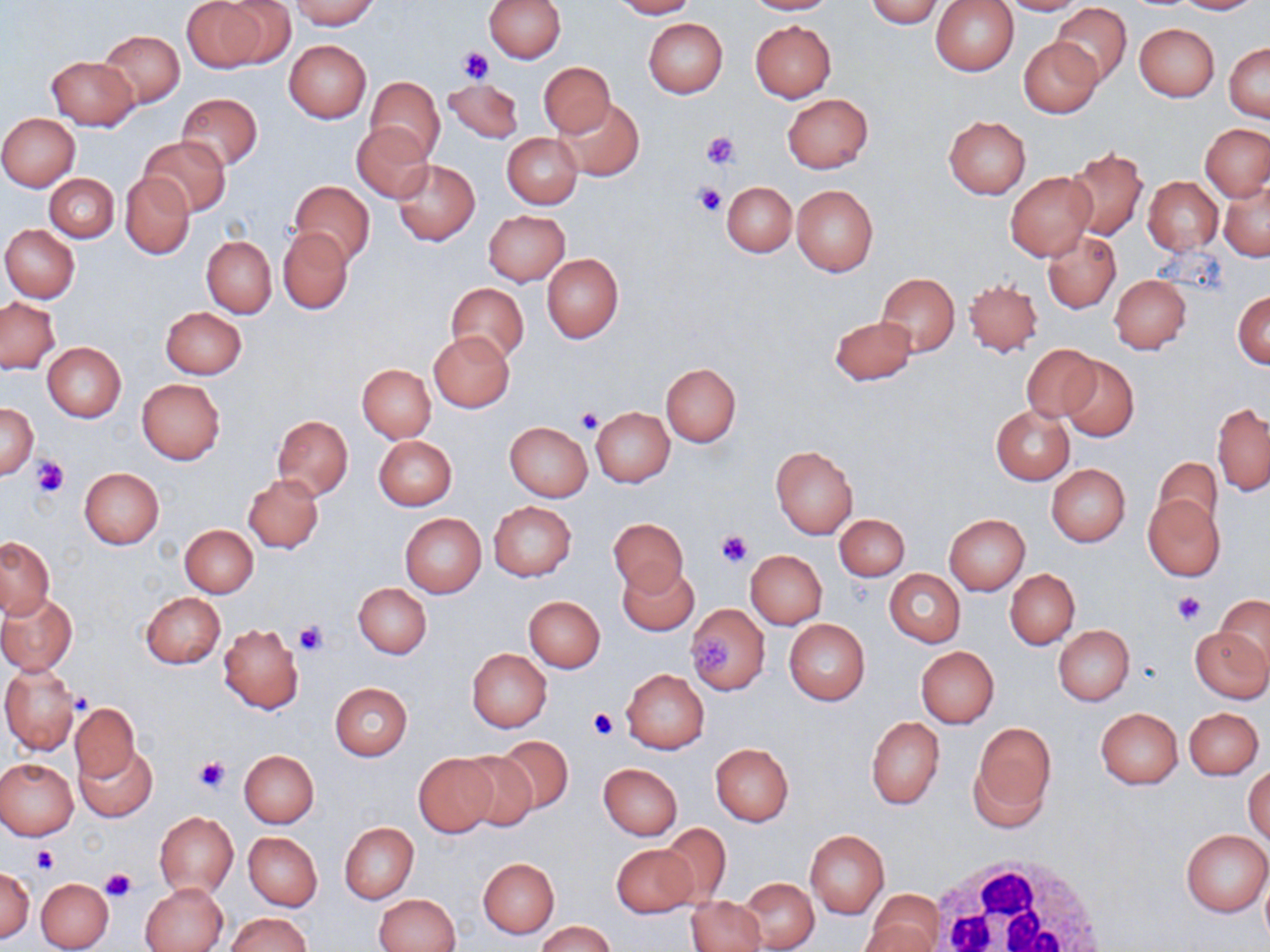
Summary:
  - Coordinate format: approximate bounding boxes as (x1, y1, x2, y2) in pixels
  - Uninfected red blood cell locations: (183, 0, 268, 72), (215, 0, 297, 68), (289, 0, 379, 30), (485, 0, 565, 62), (611, 0, 697, 18), (744, 0, 835, 15), (865, 0, 945, 27), (930, 0, 1019, 76), (998, 0, 1087, 15), (1174, 0, 1259, 14), (1050, 3, 1133, 87), (644, 19, 727, 99), (750, 21, 836, 102), (1134, 23, 1219, 100), (98, 29, 185, 108), (1019, 37, 1103, 117), (284, 40, 372, 123), (1225, 43, 1270, 122), (46, 56, 139, 130), (539, 62, 615, 137), (365, 76, 444, 162), (442, 78, 523, 144), (176, 92, 262, 172), (783, 93, 873, 173), (556, 97, 645, 181), (0, 113, 80, 191), (944, 116, 1031, 198), (352, 122, 433, 203), (1201, 123, 1269, 200), (502, 132, 582, 208), (140, 136, 230, 217), (1065, 149, 1148, 238), (392, 159, 479, 246), (1005, 172, 1096, 262), (121, 173, 194, 259), (45, 174, 119, 243), (1142, 177, 1222, 254), (290, 180, 375, 266), (1219, 180, 1270, 261), (722, 182, 795, 256), (791, 184, 879, 275), (484, 210, 570, 286), (1, 224, 80, 302), (279, 227, 353, 313), (1043, 231, 1120, 313), (202, 236, 276, 317), (542, 253, 623, 342), (877, 274, 959, 356), (1109, 275, 1191, 354), (964, 280, 1043, 356), (446, 282, 528, 365), (1233, 290, 1270, 368), (1, 298, 60, 373), (161, 306, 247, 379), (829, 314, 917, 385), (429, 331, 514, 412), (43, 342, 126, 420), (1021, 343, 1101, 422), (1059, 356, 1139, 442), (660, 363, 742, 447), (358, 364, 435, 442), (136, 379, 226, 464), (1, 403, 37, 477), (1212, 403, 1269, 494), (991, 405, 1075, 483), (591, 406, 674, 488), (272, 415, 353, 498), (505, 421, 592, 501), (375, 436, 456, 510), (770, 444, 858, 539), (1151, 457, 1222, 538), (1046, 464, 1130, 546), (79, 467, 165, 548), (243, 474, 324, 553), (1143, 495, 1223, 581), (488, 501, 577, 581), (400, 514, 486, 597), (834, 514, 909, 580), (944, 514, 1029, 594), (609, 517, 688, 595), (180, 524, 258, 597), (2, 536, 54, 619), (746, 550, 826, 628), (618, 562, 698, 636), (885, 568, 965, 647), (1005, 568, 1080, 649), (354, 582, 431, 659), (139, 592, 226, 669), (0, 594, 77, 674), (524, 596, 605, 672), (1216, 596, 1270, 672), (686, 603, 770, 695), (784, 619, 870, 706), (218, 623, 303, 713), (1053, 625, 1134, 705), (1190, 626, 1270, 702), (916, 646, 998, 727), (466, 648, 552, 732), (1, 664, 82, 754), (621, 668, 709, 754), (328, 681, 412, 760), (69, 703, 140, 781), (1185, 707, 1263, 779), (1097, 708, 1182, 788), (866, 716, 944, 808), (971, 723, 1055, 820), (493, 735, 573, 814), (709, 742, 794, 826), (76, 744, 156, 821), (239, 750, 319, 827), (456, 751, 542, 832), (412, 753, 500, 837), (0, 757, 78, 839), (598, 762, 682, 839), (1244, 763, 1270, 844), (155, 812, 238, 897), (339, 822, 418, 904), (658, 822, 732, 905), (805, 829, 889, 919), (1181, 829, 1269, 916), (244, 832, 322, 910), (610, 844, 700, 917), (478, 857, 560, 937), (0, 866, 35, 941), (1259, 871, 1270, 945), (36, 878, 113, 951), (740, 878, 819, 951), (140, 882, 228, 952), (870, 889, 945, 949), (374, 893, 460, 952), (687, 896, 766, 952), (228, 913, 311, 952), (536, 921, 617, 952), (859, 924, 936, 952)
  - White blood cell locations: (924, 851, 1112, 952)
  - Platelet locations: (458, 47, 496, 85), (702, 131, 741, 169), (693, 184, 725, 217), (576, 408, 602, 434), (33, 454, 68, 495), (716, 531, 752, 568), (1173, 591, 1207, 626), (296, 620, 328, 656), (692, 632, 732, 675), (587, 709, 617, 739), (194, 755, 228, 792), (32, 845, 58, 873), (100, 867, 136, 902)
  - Slide-level diagnosis: negative for blood parasites
  - Stain: May-Grünwald-Giemsa
  - Field of view: one of a larger specimen
  - Image size: 1270×952 pixels
  - Magnification: 1000x
  - Preparation: thin blood smear
  - Modality: light microscopy